Describe the morphology of the erythrocytes.
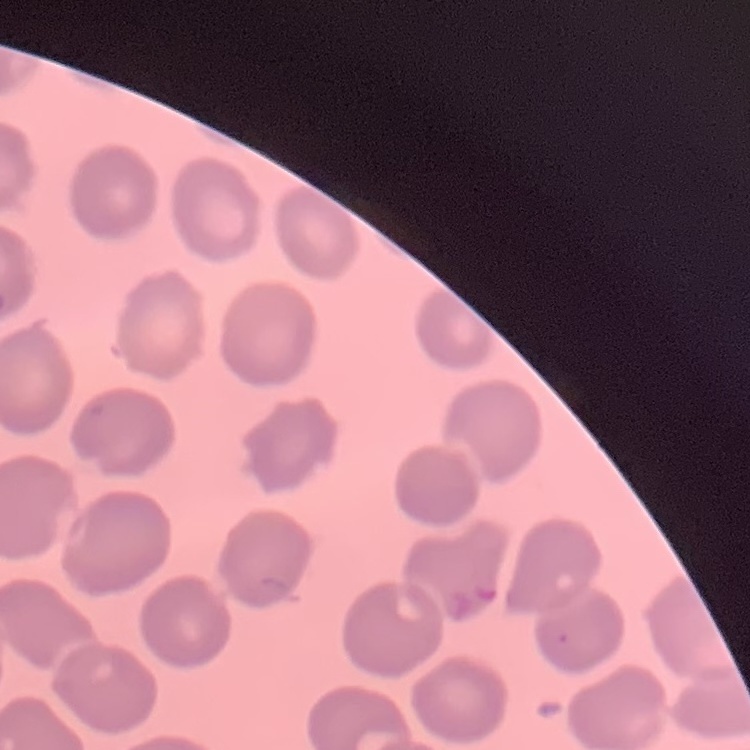

No rouleaux formation.

Stained with either Field's or Giemsa. Square crop of a larger photomicrograph. Thin blood smear.